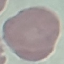 Malaria status: uninfected. Cell patch, automatically extracted from a larger field of view and resized to 64 × 64 pixels. Photographed with a smartphone camera at the microscope eyepiece. Thin blood smear. Giemsa-stained preparation.